Point out each malaria parasite and classify it by life-cycle stage.
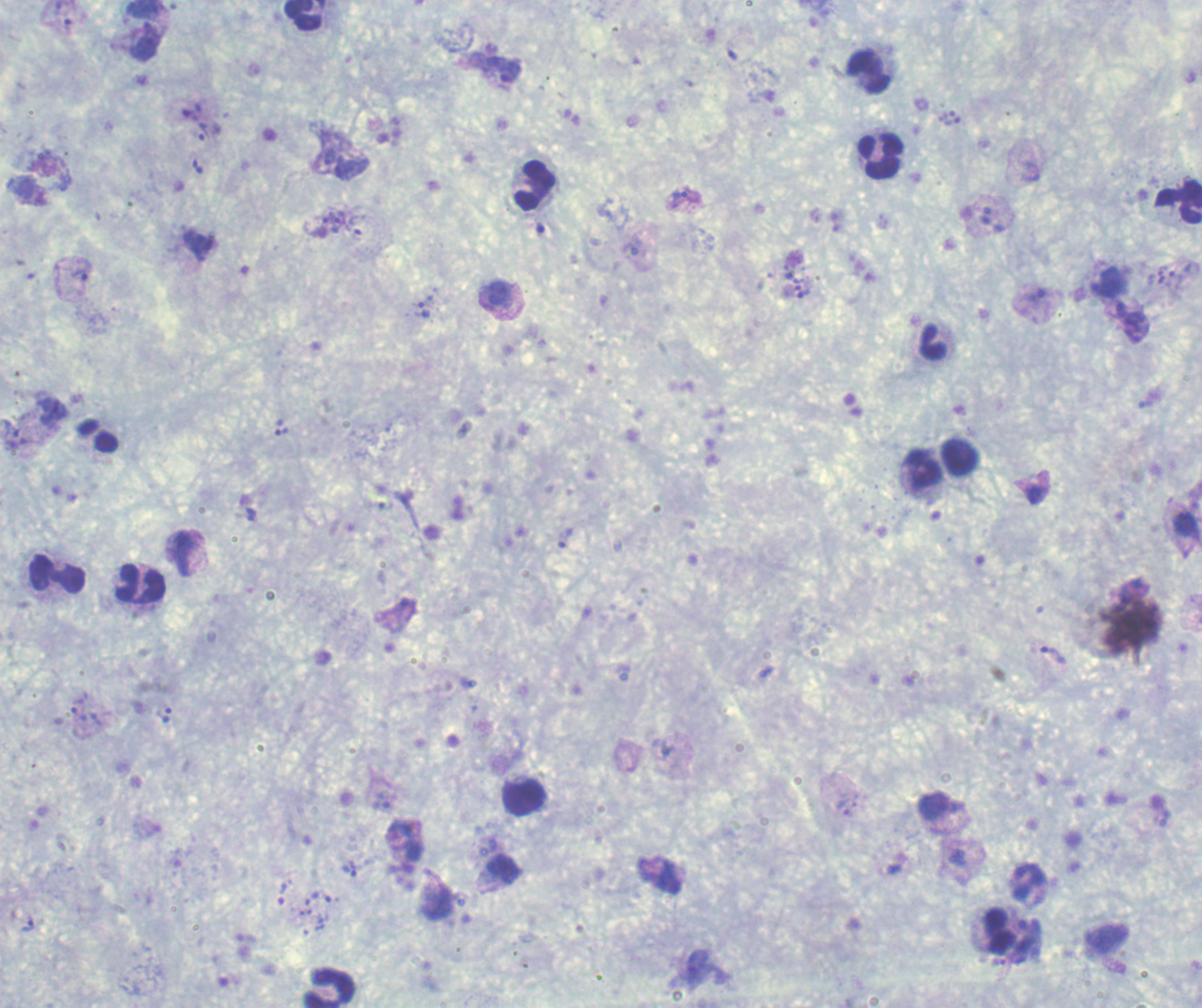
Approximate object centers, in pixels from the top-left corner.
Trophozoites: (x=68, y=25), (x=145, y=45), (x=511, y=72), (x=191, y=109), (x=946, y=114), (x=953, y=120), (x=203, y=131), (x=329, y=156), (x=1031, y=173), (x=679, y=198), (x=337, y=220), (x=321, y=226), (x=197, y=245), (x=81, y=271), (x=1160, y=276), (x=1176, y=280), (x=1107, y=281), (x=804, y=294), (x=423, y=310), (x=1132, y=322), (x=1149, y=398), (x=281, y=428), (x=1036, y=494), (x=250, y=514), (x=565, y=538), (x=1053, y=655), (x=77, y=705), (x=167, y=715), (x=844, y=808), (x=349, y=868), (x=27, y=926), (x=1030, y=928), (x=999, y=962).
Schizonts: (x=958, y=857), (x=505, y=868).
No gametocyte forms observed.

Approximate object centers, in pixels from the top-left corner. Leukocyte locations: (x=303, y=18), (x=867, y=71), (x=880, y=157), (x=532, y=185), (x=1178, y=200), (x=932, y=344), (x=959, y=457), (x=922, y=472), (x=56, y=572), (x=140, y=585), (x=524, y=797), (x=995, y=930), (x=327, y=987). Romanowsky-stained preparation. Previously used in a real diagnosis. 100x magnification. Background quality: satisfactory. Image is 1202×1008 pixels. Single field of view. Thick blood film.